Comment on the morphology of the erythrocytes.
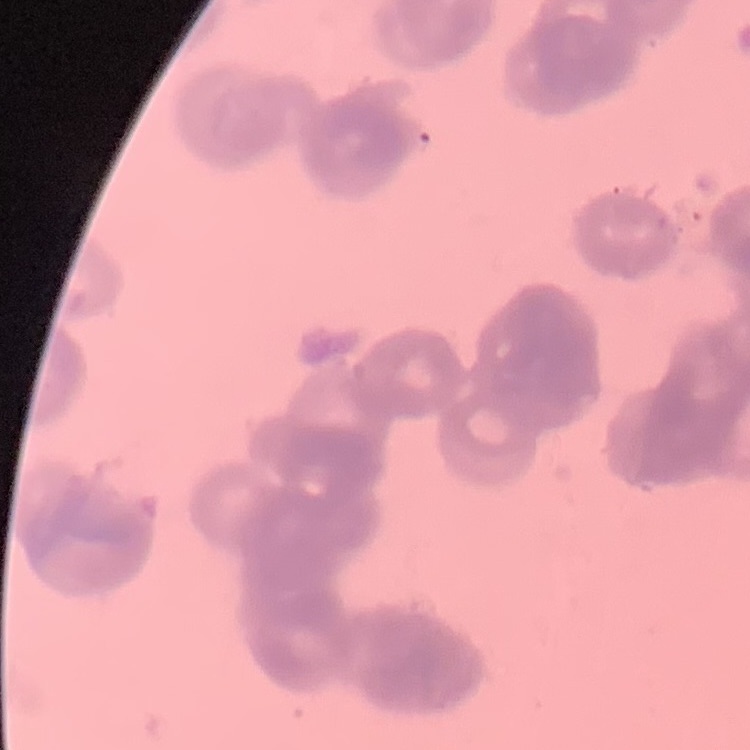
Rouleaux formation.

Summary:
  - Preparation: thin blood smear
  - Stain: Field's or Giemsa
  - Image type: square crop of a larger photomicrograph